Name the cell type shown.
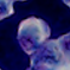

A leukocyte.

Summary:
  - Modality: micrograph
  - Magnification: 1000x